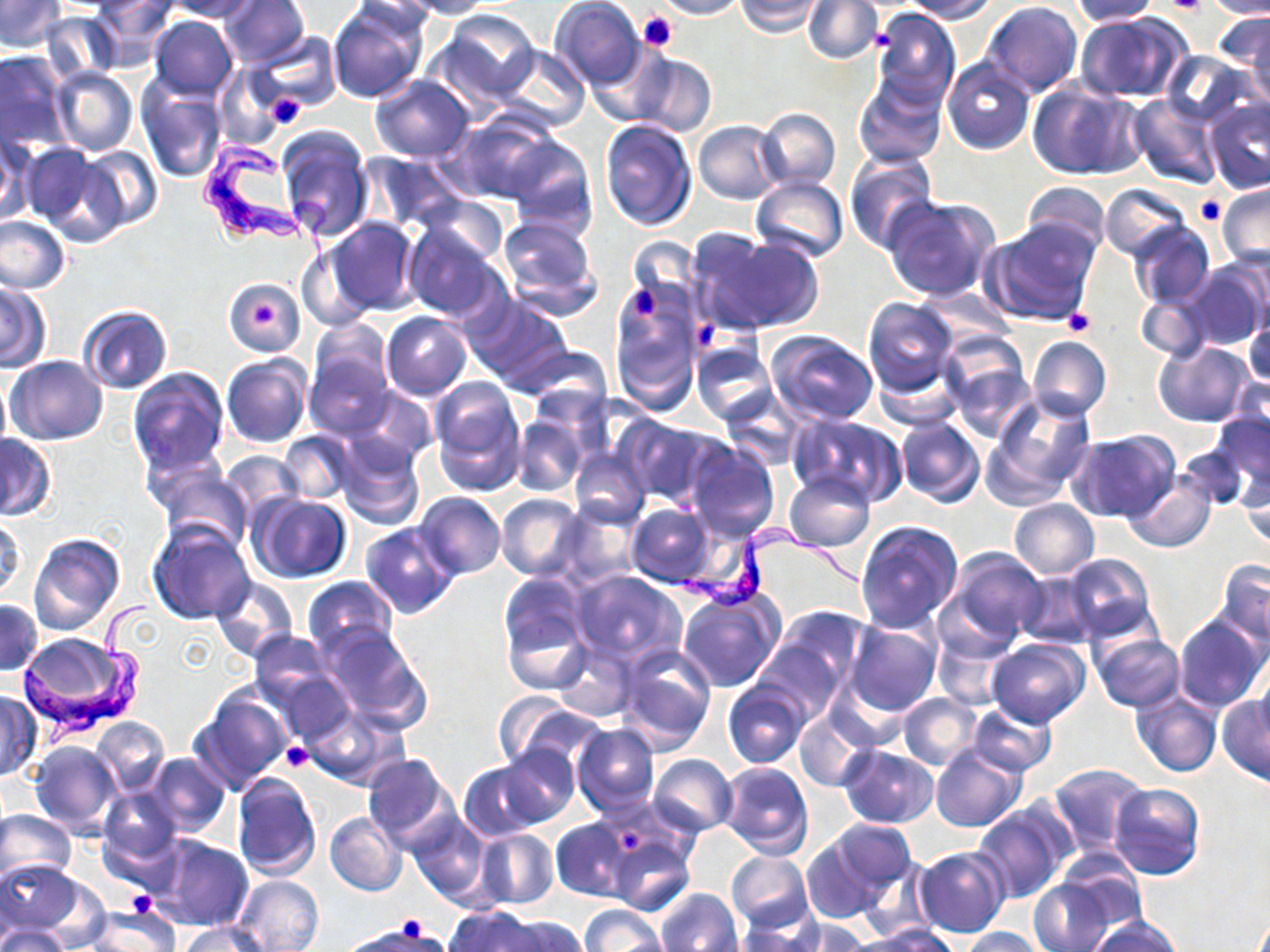

Approximate bounding boxes as [x1, y1, x2, y2] in pixels. Platelet locations: [1159, 0, 1210, 16], [638, 10, 677, 53], [262, 91, 310, 129], [1197, 196, 1226, 224], [629, 288, 658, 322], [252, 302, 278, 327], [1063, 309, 1096, 337], [692, 318, 719, 349], [283, 741, 314, 772], [620, 825, 648, 851], [125, 892, 155, 916], [395, 918, 433, 950]. Uninfected red blood cell locations: [0, 0, 66, 51], [90, 0, 177, 67], [167, 0, 258, 21], [218, 0, 309, 70], [403, 0, 494, 19], [655, 0, 746, 20], [735, 0, 823, 36], [803, 0, 883, 64], [900, 0, 998, 21], [1205, 0, 1270, 19], [328, 1, 427, 104], [550, 1, 645, 91], [984, 1, 1082, 96], [1068, 1, 1159, 25], [6, 2, 114, 63], [871, 8, 960, 111], [439, 10, 541, 107], [1219, 10, 1270, 105], [39, 11, 121, 84], [1074, 12, 1192, 103], [150, 15, 238, 101], [253, 32, 342, 117], [589, 43, 680, 129], [497, 44, 589, 133], [0, 50, 71, 152], [1159, 50, 1255, 128], [630, 53, 716, 137], [942, 57, 1035, 154], [217, 65, 286, 146], [53, 68, 137, 156], [371, 76, 475, 163], [853, 76, 946, 168], [1027, 80, 1145, 181], [136, 81, 227, 183], [1127, 93, 1221, 188], [1202, 99, 1270, 195], [756, 106, 843, 192], [448, 112, 559, 205], [598, 120, 696, 232], [693, 120, 785, 204], [278, 125, 373, 241], [0, 132, 32, 225], [504, 136, 597, 238], [29, 146, 127, 244], [79, 146, 163, 231], [365, 152, 469, 231], [844, 152, 937, 253], [751, 175, 849, 262], [1019, 181, 1110, 258], [1217, 182, 1270, 273], [1100, 184, 1190, 261], [424, 195, 509, 265], [883, 197, 999, 303], [0, 215, 70, 294], [495, 215, 602, 321], [327, 217, 421, 317], [985, 219, 1098, 325], [1126, 221, 1213, 309], [403, 223, 504, 322], [689, 229, 817, 334], [299, 245, 378, 330], [1178, 262, 1268, 353], [1, 281, 50, 371], [226, 282, 302, 353], [611, 283, 705, 413], [1133, 290, 1211, 361], [463, 294, 572, 391], [862, 296, 960, 397], [76, 305, 172, 392], [381, 312, 471, 398], [1243, 314, 1270, 392], [309, 319, 392, 403], [765, 330, 878, 425], [1027, 336, 1111, 422], [692, 340, 776, 425], [1153, 341, 1255, 427], [944, 342, 1036, 440], [517, 345, 615, 420], [305, 348, 394, 440], [222, 355, 310, 448], [7, 356, 108, 445], [873, 359, 965, 433], [129, 369, 229, 476], [0, 375, 11, 454], [429, 377, 526, 493], [347, 387, 436, 470], [719, 391, 803, 471], [985, 391, 1098, 501], [1210, 406, 1269, 505], [789, 415, 907, 507], [512, 416, 589, 497], [620, 416, 722, 508], [895, 416, 984, 507], [1067, 430, 1179, 523], [278, 431, 356, 503], [335, 434, 425, 529], [0, 435, 55, 519], [1177, 440, 1251, 513], [684, 441, 781, 544], [569, 449, 650, 528], [220, 452, 303, 522], [157, 468, 252, 551], [782, 470, 875, 552], [1239, 470, 1270, 554], [1125, 472, 1216, 552], [415, 492, 506, 579], [248, 493, 353, 583], [497, 493, 586, 581], [1008, 498, 1099, 579], [555, 503, 644, 589], [626, 504, 718, 588], [1, 516, 26, 604], [855, 520, 965, 633], [147, 521, 254, 626], [359, 522, 459, 619], [28, 532, 124, 635], [945, 548, 1047, 644], [1061, 553, 1157, 644], [1213, 559, 1270, 646], [570, 571, 684, 669], [1017, 572, 1097, 649], [211, 576, 298, 661], [302, 576, 397, 660], [676, 588, 783, 692], [500, 594, 592, 695], [0, 600, 41, 676], [764, 605, 872, 700], [1174, 613, 1267, 713], [847, 620, 942, 719], [320, 627, 432, 731], [933, 627, 1016, 710], [247, 630, 335, 714], [1090, 632, 1185, 711], [987, 638, 1089, 729], [550, 640, 634, 722], [615, 644, 716, 753], [263, 659, 357, 744], [1255, 662, 1270, 745], [723, 680, 811, 770], [194, 687, 293, 793], [1130, 688, 1222, 777], [1, 691, 40, 781], [896, 692, 982, 769], [1217, 695, 1270, 785], [496, 698, 601, 772], [968, 701, 1056, 775], [303, 706, 407, 789], [794, 712, 872, 792], [93, 716, 169, 794], [572, 723, 659, 816], [28, 740, 123, 839], [931, 744, 1026, 833], [498, 745, 580, 827], [838, 746, 939, 829], [146, 753, 230, 837], [361, 754, 459, 852], [648, 754, 737, 836], [719, 761, 812, 858], [459, 762, 549, 841], [1047, 763, 1147, 858], [232, 772, 321, 881], [1109, 782, 1204, 879], [99, 786, 184, 872], [972, 801, 1073, 903], [0, 809, 75, 885], [326, 811, 407, 897], [409, 813, 491, 905], [551, 819, 633, 902], [801, 825, 911, 923], [474, 828, 558, 910], [603, 828, 696, 915], [153, 836, 253, 931], [915, 848, 1010, 938], [724, 851, 813, 932], [1058, 857, 1147, 937], [0, 858, 84, 940], [234, 875, 325, 951], [1027, 878, 1116, 951], [655, 887, 743, 952], [579, 904, 668, 952], [85, 905, 180, 951], [443, 908, 543, 952], [1085, 915, 1184, 952], [497, 916, 587, 952], [733, 918, 823, 951], [780, 919, 870, 951], [0, 922, 69, 952], [177, 923, 272, 952], [343, 923, 440, 951], [860, 925, 959, 952], [959, 927, 1050, 951]. Trypanosoma brucei locations: [198, 134, 338, 280], [653, 520, 868, 623], [18, 599, 148, 742]. Slide-level diagnosis: Trypanosoma brucei. 1000x magnification. Image is 1270×952 pixels. Thin blood smear. One field of a larger specimen. May-Grünwald-Giemsa stain. Light microscopy.